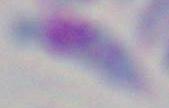
Summary:
  - Magnification: 1000x
  - Modality: photomicrograph
  - Identification: Toxoplasma gondii